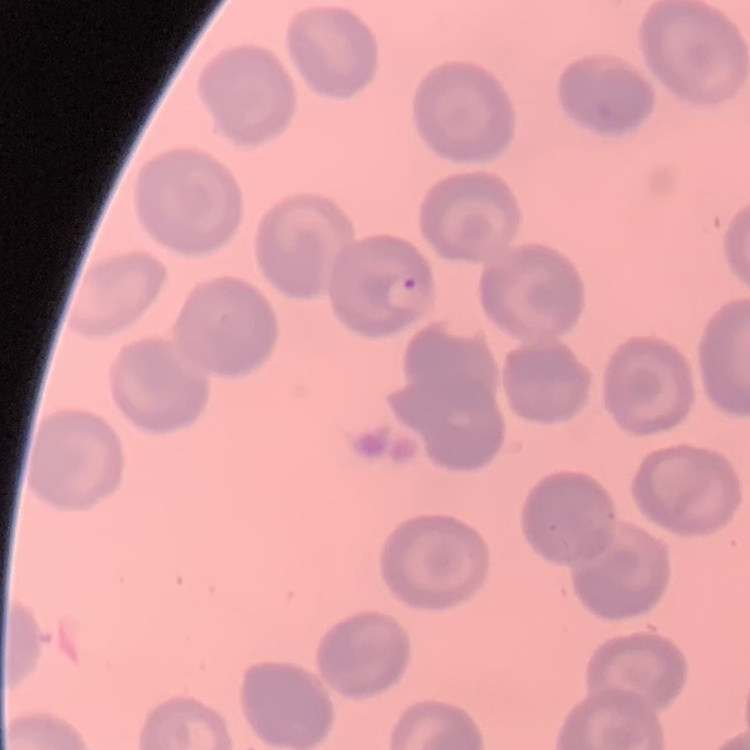
{
  "red_blood_cell_morphology": "no rouleaux formation",
  "stain": "Field's or Giemsa",
  "image_type": "one tile cut from a larger photomicrograph",
  "preparation": "thin blood film"
}